Report the malaria status of this cell.
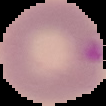

Parasitized.

{
  "image_type": "cell region segmented out of the field of view; surrounding area masked to black",
  "preparation": "thin blood film",
  "image_size": "106×106 pixels"
}